Outline each blood parasite and name the species.
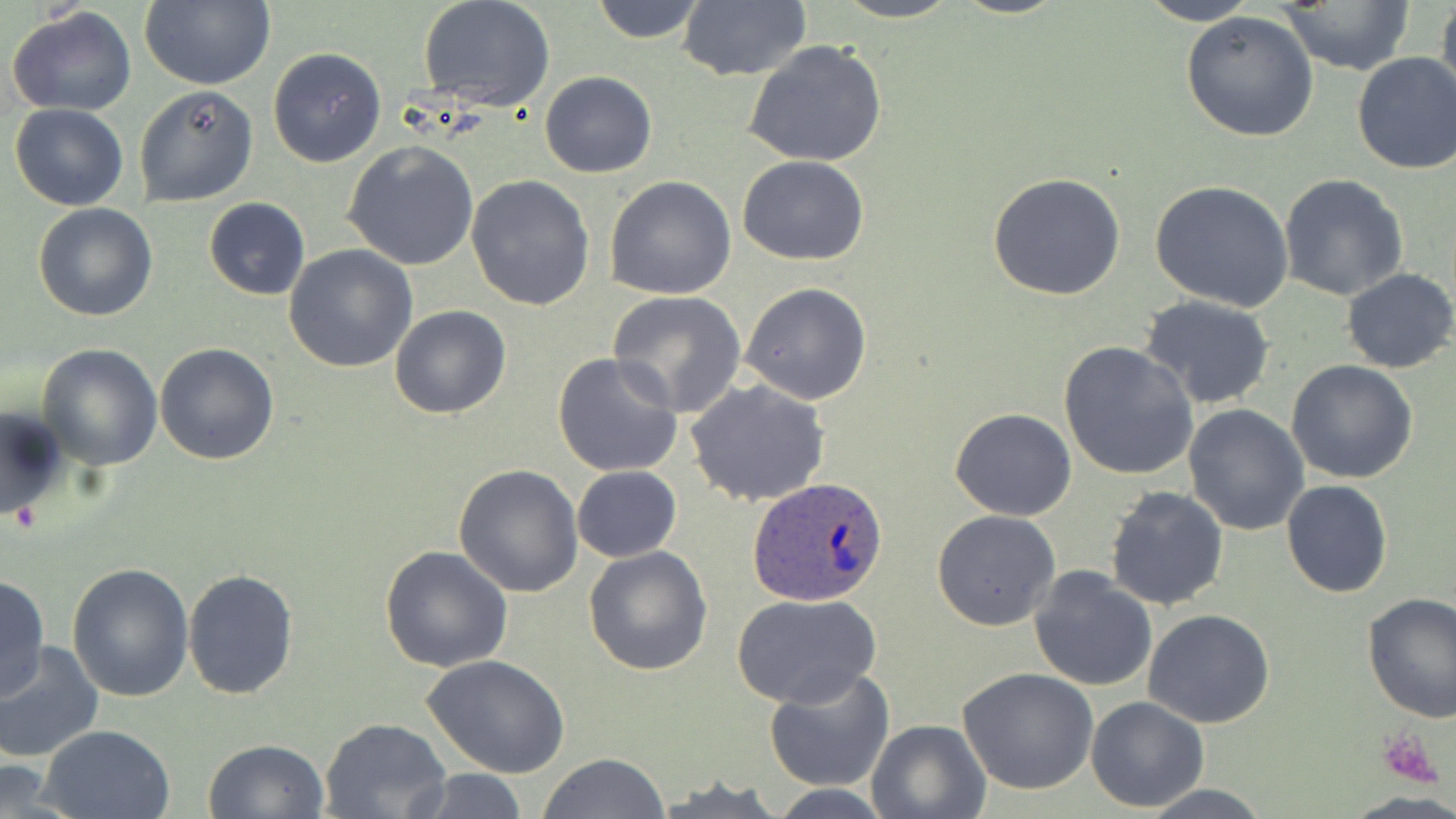
Approximate bounding boxes as (x1,y1)-(x2,y2) corner pairs in pixels.
Plasmodium ovale-infected red blood cells: (747,476)-(890,609).
No Plasmodium falciparum, Plasmodium malariae, Plasmodium vivax, Babesia divergens, or Trypanosoma brucei observed.

slide_level_diagnosis: Plasmodium ovale
uninfected_red_blood_cell_locations: 'approximate bounding boxes as (x1,y1)-(x2,y2) corner pairs in pixels: (588,0)-(708,44), (827,0)-(963,23), (1134,0)-(1263,25), (1436,0)-(1456,111), (139,1)-(275,90), (419,1)-(554,112), (1273,1)-(1420,74), (677,3)-(812,82), (6,7)-(137,117), (1179,9)-(1319,142), (743,39)-(889,167), (266,46)-(387,169), (1351,52)-(1456,175), (538,70)-(657,178), (133,83)-(258,208), (9,103)-(129,212), (343,140)-(479,270), (737,155)-(869,266), (987,171)-(1129,302), (1277,174)-(1409,301), (467,175)-(595,312), (605,175)-(736,300), (1150,180)-(1295,312), (203,198)-(310,300), (33,202)-(158,322), (285,244)-(417,373), (1341,268)-(1456,374), (739,281)-(874,405), (608,291)-(747,417), (1140,296)-(1276,409), (390,304)-(510,419), (1059,341)-(1198,480), (153,343)-(280,466), (36,344)-(163,470), (552,352)-(685,479), (1286,361)-(1419,483), (686,377)-(831,506), (0,405)-(72,525), (1183,405)-(1309,535), (950,407)-(1076,521), (453,464)-(584,597), (571,466)-(681,562), (1280,479)-(1393,599), (1103,483)-(1230,610), (932,509)-(1060,632), (380,545)-(513,672), (584,546)-(712,678), (68,562)-(196,702), (1027,567)-(1158,692), (183,568)-(300,699), (1,575)-(50,701), (733,592)-(883,711), (1361,592)-(1456,721), (1143,609)-(1276,729), (0,642)-(104,763), (422,654)-(571,778), (958,666)-(1099,795), (763,667)-(895,793), (1087,695)-(1209,814), (320,716)-(453,819), (866,718)-(989,818), (37,725)-(177,818), (203,738)-(329,819), (538,752)-(671,819), (0,760)-(71,813), (405,768)-(533,818), (1134,782)-(1275,817)'
stain: May-Grünwald-Giemsa
modality: light microscopy
magnification: 1000x
field_of_view: single
preparation: thin blood smear
image_size: 1456×819 pixels
platelet_locations: 'approximate bounding boxes as (x1,y1)-(x2,y2) corner pairs in pixels: (1377,730)-(1442,787)'